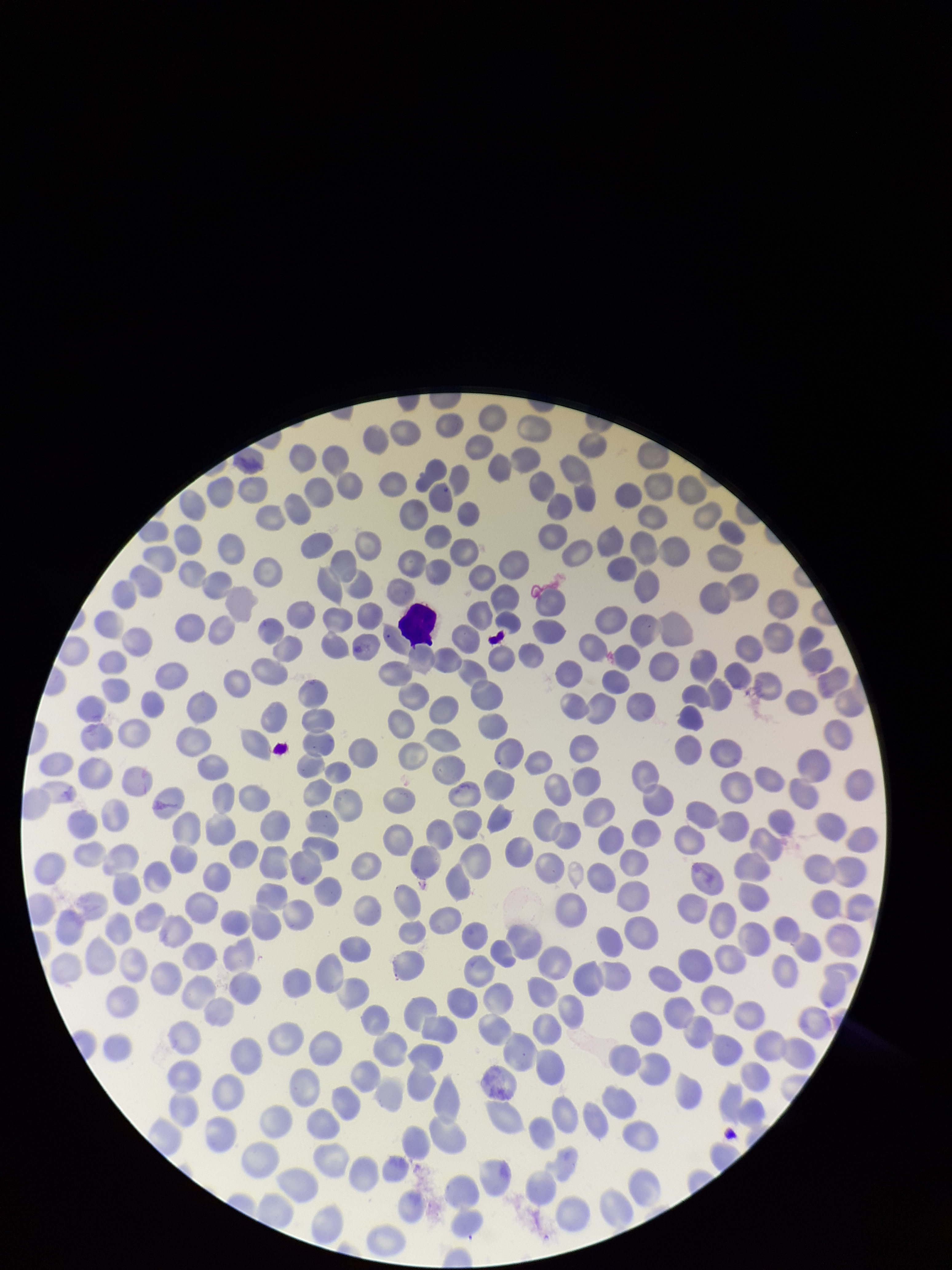
Summary:
  - Parasitized red blood cell count: 0
  - Capture: smartphone photograph through the microscope eyepiece
  - Parasitized red blood cells: none seen
  - Field of view: one from this slide
  - Stain: Giemsa
  - Red blood cell count: 309
  - Image size: 952×1270 pixels
  - Preparation: thin smear
  - Patient malaria status: negative